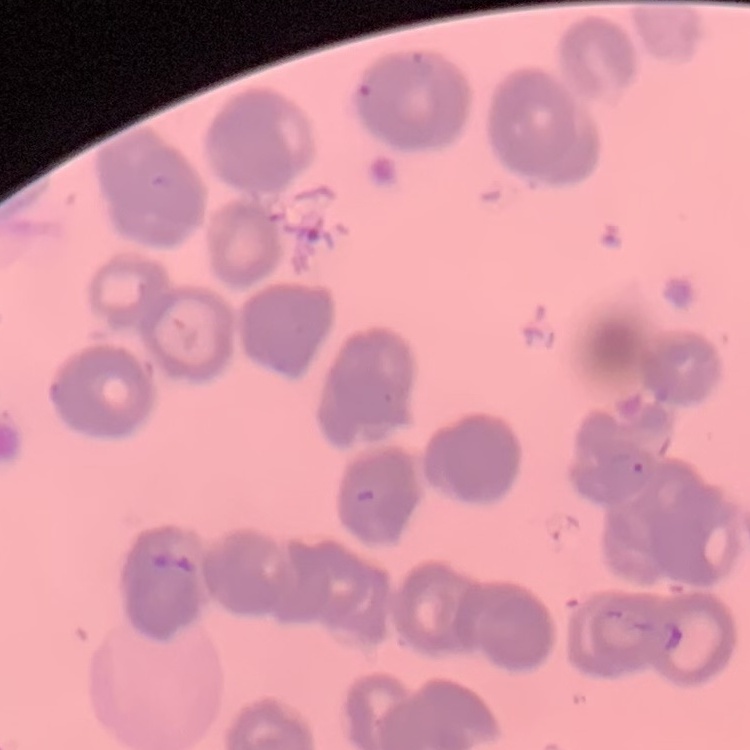
red blood cell morphology = rouleaux formation
preparation = thin blood film
image type = square crop of a larger photomicrograph
stain = Field's or Giemsa